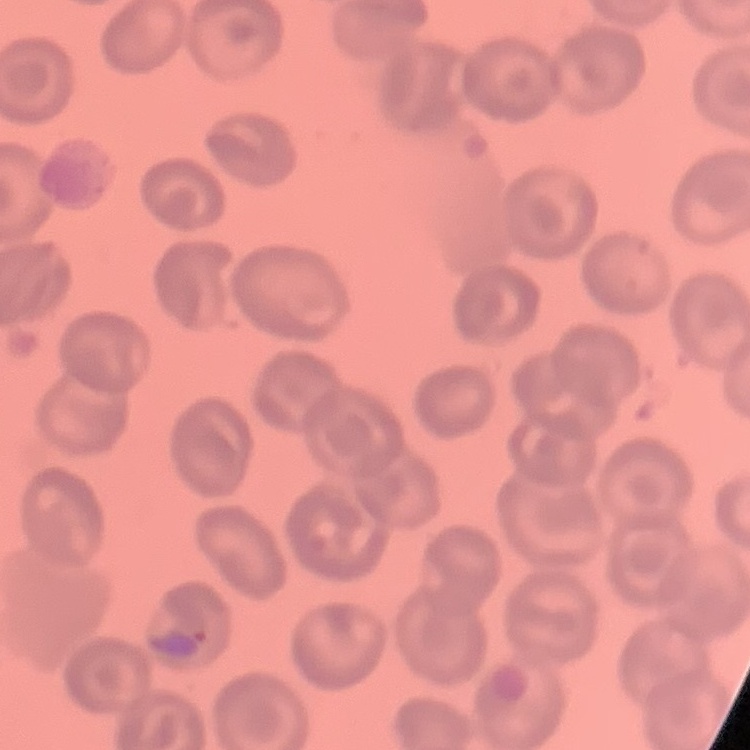
erythrocyte morphology = no rouleaux formation
stain = Field's or Giemsa
preparation = thin blood smear
image type = one tile cut from a larger photomicrograph